Assess the morphology of the red blood cells.
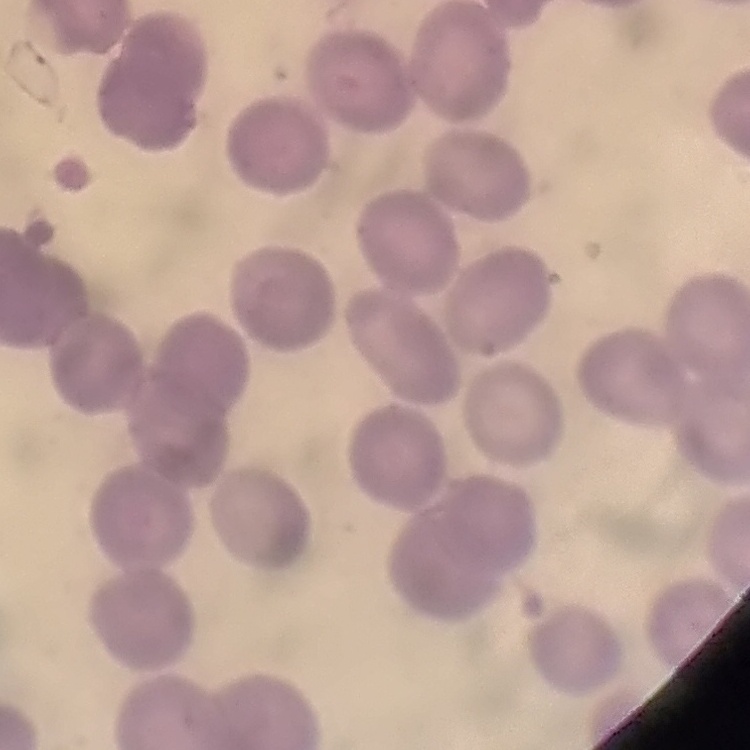

No rouleaux formation.

Field's or Giemsa stain. Thin blood smear. One tile cut from a larger photomicrograph.